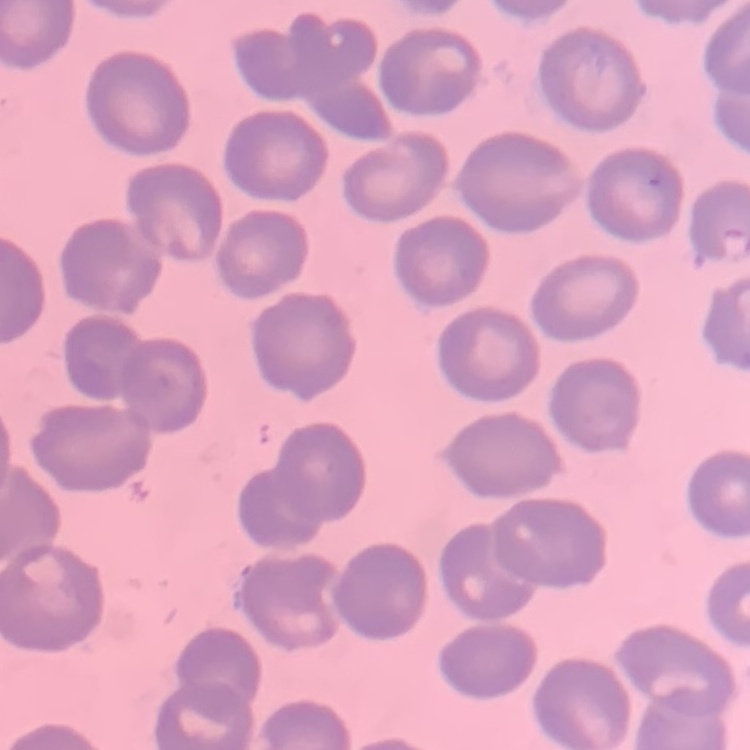

Summary:
  - Red blood cell morphology: no rouleaux formation
  - Preparation: thin blood smear
  - Image type: one tile cut from a larger photomicrograph
  - Stain: Field's or Giemsa